Locate every Plasmodium vivax-infected red blood cell.
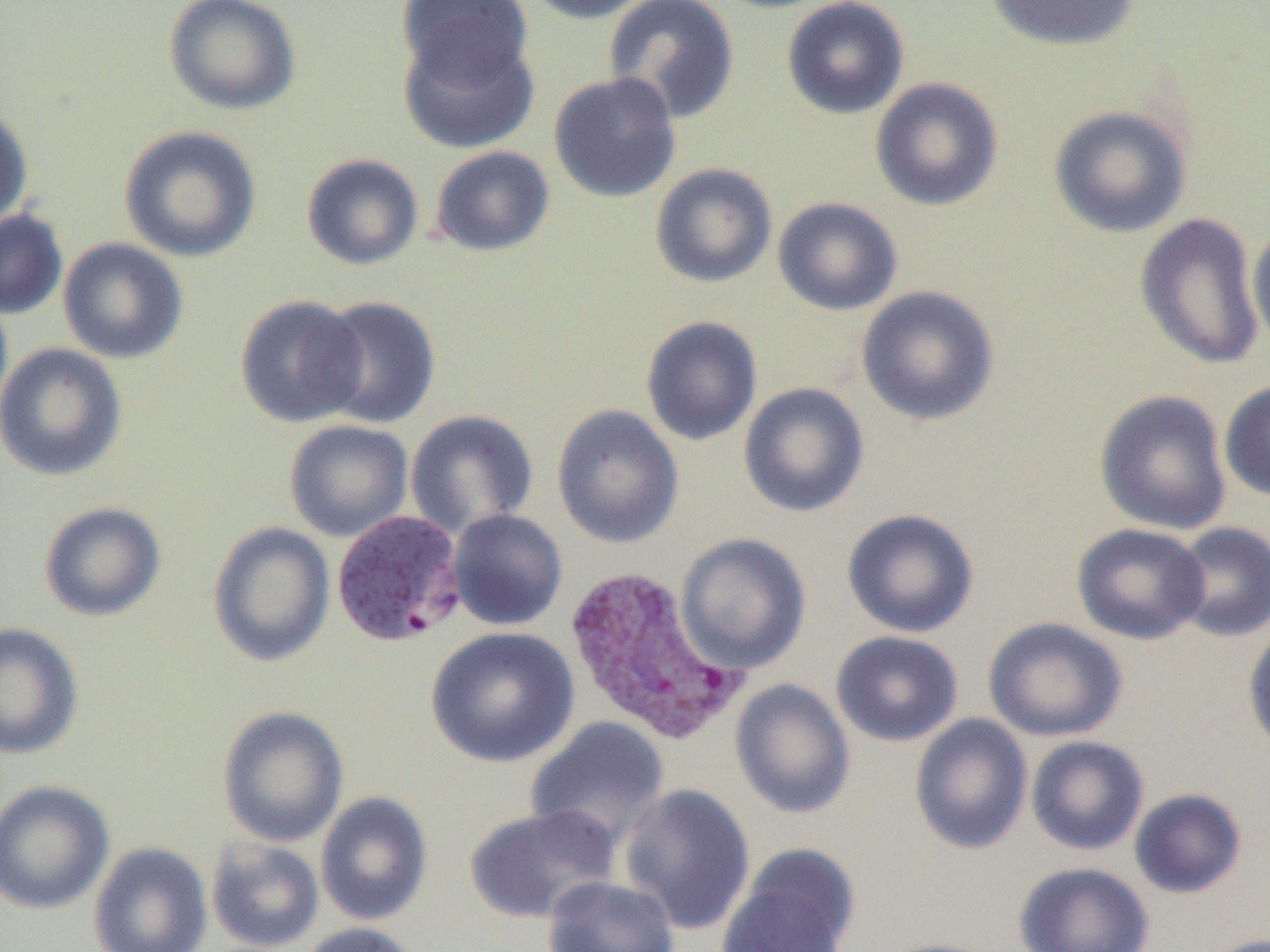
Approximate bounding boxes as (x1, y1, x2, y2) in pixels.
Plasmodium vivax-infected red blood cells: (330, 510, 467, 647), (561, 564, 750, 747).

{
  "slide_level_diagnosis": "Plasmodium vivax",
  "modality": "light microscopy",
  "image_size": "1270×952 pixels",
  "field_of_view": "single",
  "preparation": "thin blood film",
  "magnification": "1000x",
  "uninfected_red_blood_cell_locations": "approximate bounding boxes as (x1, y1, x2, y2) in pixels: (163, 0, 301, 116), (397, 0, 532, 87), (520, 0, 660, 24), (603, 0, 740, 124), (782, 0, 910, 120), (983, 0, 1142, 52), (397, 26, 540, 154), (548, 72, 682, 204), (869, 77, 1004, 212), (0, 104, 33, 230), (1049, 105, 1192, 238), (119, 125, 262, 263), (429, 145, 556, 257), (302, 154, 424, 270), (650, 162, 777, 288), (772, 197, 903, 316), (0, 209, 68, 319), (1134, 213, 1266, 371), (1247, 221, 1270, 356), (57, 238, 189, 365), (856, 286, 1000, 426), (234, 294, 369, 427), (314, 295, 441, 429), (641, 315, 763, 446), (0, 343, 127, 481), (1219, 379, 1270, 501), (738, 382, 870, 518), (1094, 390, 1232, 535), (551, 404, 684, 549), (405, 409, 539, 538), (284, 420, 413, 541), (38, 502, 166, 622), (842, 508, 979, 638), (447, 509, 568, 631), (207, 521, 335, 666), (1171, 521, 1270, 643), (1071, 523, 1210, 645), (675, 533, 811, 674), (983, 617, 1127, 742), (1242, 621, 1270, 758), (0, 622, 83, 759), (426, 626, 580, 767), (830, 630, 963, 747), (730, 678, 855, 819), (216, 705, 350, 847), (910, 714, 1033, 855), (525, 716, 670, 850), (1026, 735, 1149, 856), (0, 779, 115, 915), (618, 783, 755, 936), (1128, 788, 1248, 899), (315, 791, 433, 926), (463, 804, 620, 924), (205, 837, 324, 952), (88, 842, 212, 952), (716, 850, 859, 952), (1013, 861, 1154, 952), (542, 875, 680, 952), (297, 922, 424, 952), (1201, 933, 1270, 952), (869, 938, 1005, 952)"
}